Name the parasite shown.
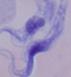

A trypanosome.

1000x magnification. Micrograph.